Identify the cell.
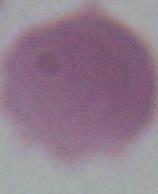

This is an erythrocyte.

Summary:
  - Modality: photomicrograph
  - Magnification: 1000x